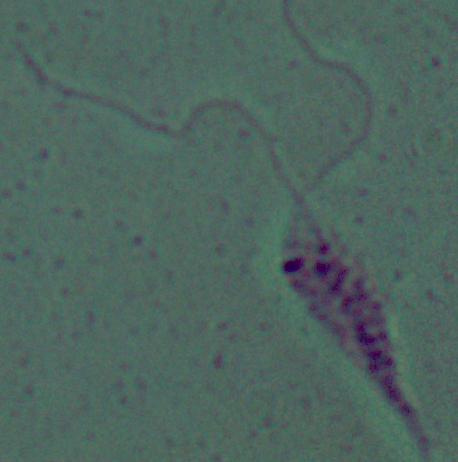 A Leishmania parasite is shown. Micrograph. Captured at 1000x magnification.